Report the malaria status of this cell.
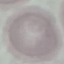

It is uninfected.

Summary:
  - Image type: cell patch, automatically extracted from a larger field of view and resized to 64 × 64 pixels
  - Capture: smartphone through the microscope eyepiece
  - Stain: Giemsa
  - Preparation: thin blood film